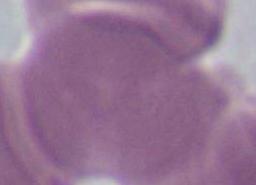

modality = photomicrograph
identification = erythrocyte
magnification = 1000x